Assess this cell for malaria.
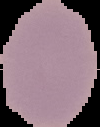
It is uninfected.

{
  "image_type": "segmented cell region on a black background",
  "preparation": "thin blood smear",
  "image_size": "100×127 pixels"
}